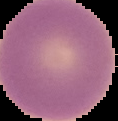
Cell region segmented out of the field of view; the surrounding area is masked to black. From a thin blood film. Malaria status: uninfected. Image is 118×121 pixels.